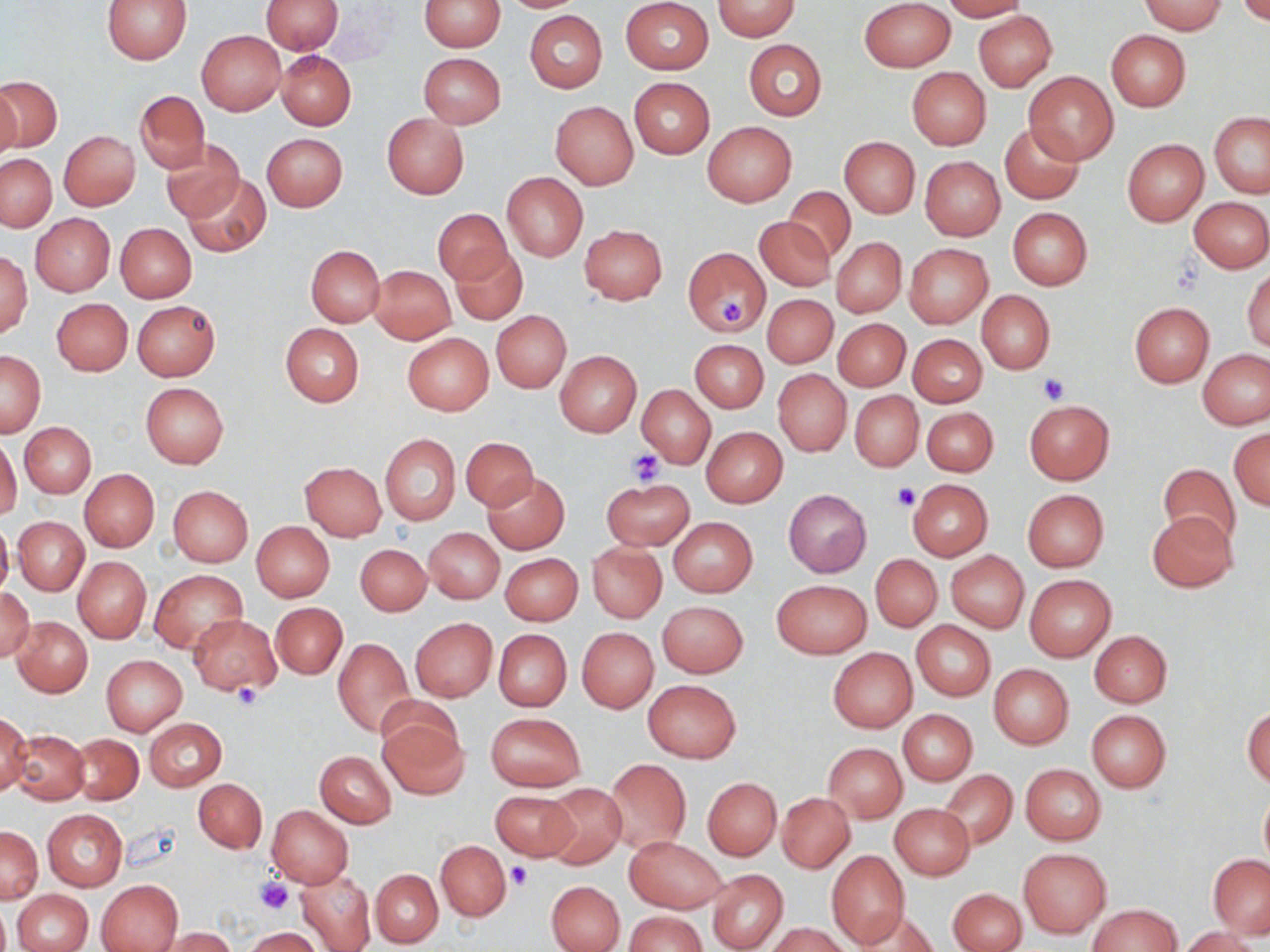

slide-level diagnosis = negative for blood parasites
stain = May-Grünwald-Giemsa
uninfected red blood cell locations = approximate bounding boxes as named x1/y1/x2/y2 corners in pixels: (x1=102, y1=0, x2=192, y2=64), (x1=261, y1=0, x2=344, y2=54), (x1=419, y1=0, x2=505, y2=51), (x1=497, y1=0, x2=591, y2=12), (x1=860, y1=0, x2=954, y2=71), (x1=942, y1=0, x2=1028, y2=21), (x1=621, y1=1, x2=713, y2=74), (x1=712, y1=1, x2=800, y2=39), (x1=1138, y1=1, x2=1227, y2=34), (x1=1235, y1=1, x2=1270, y2=24), (x1=524, y1=11, x2=606, y2=92), (x1=973, y1=11, x2=1057, y2=92), (x1=197, y1=30, x2=286, y2=115), (x1=1105, y1=30, x2=1190, y2=111), (x1=744, y1=40, x2=826, y2=121), (x1=275, y1=50, x2=356, y2=130), (x1=419, y1=53, x2=506, y2=127), (x1=907, y1=68, x2=991, y2=150), (x1=1023, y1=70, x2=1120, y2=164), (x1=0, y1=76, x2=61, y2=152), (x1=629, y1=77, x2=714, y2=158), (x1=0, y1=82, x2=20, y2=159), (x1=135, y1=90, x2=208, y2=172), (x1=550, y1=101, x2=638, y2=189), (x1=1209, y1=112, x2=1270, y2=198), (x1=382, y1=115, x2=469, y2=198), (x1=703, y1=122, x2=797, y2=206), (x1=1000, y1=122, x2=1084, y2=204), (x1=59, y1=130, x2=140, y2=211), (x1=262, y1=133, x2=348, y2=211), (x1=839, y1=137, x2=919, y2=219), (x1=161, y1=138, x2=245, y2=222), (x1=1121, y1=138, x2=1208, y2=226), (x1=1, y1=155, x2=56, y2=231), (x1=919, y1=156, x2=1006, y2=240), (x1=501, y1=172, x2=588, y2=261), (x1=182, y1=175, x2=270, y2=257), (x1=783, y1=185, x2=857, y2=263), (x1=1190, y1=197, x2=1270, y2=272), (x1=1007, y1=207, x2=1093, y2=290), (x1=434, y1=208, x2=513, y2=284), (x1=30, y1=213, x2=115, y2=297), (x1=756, y1=215, x2=835, y2=291), (x1=115, y1=223, x2=197, y2=303), (x1=579, y1=224, x2=668, y2=304), (x1=832, y1=238, x2=906, y2=317), (x1=904, y1=243, x2=993, y2=328), (x1=306, y1=244, x2=385, y2=327), (x1=451, y1=245, x2=527, y2=325), (x1=683, y1=246, x2=771, y2=336), (x1=1, y1=249, x2=32, y2=339), (x1=370, y1=265, x2=455, y2=343), (x1=1243, y1=269, x2=1270, y2=353), (x1=977, y1=290, x2=1055, y2=374), (x1=763, y1=294, x2=838, y2=368), (x1=53, y1=299, x2=132, y2=375), (x1=132, y1=301, x2=220, y2=381), (x1=1129, y1=302, x2=1214, y2=387), (x1=492, y1=311, x2=570, y2=392), (x1=832, y1=318, x2=909, y2=391), (x1=281, y1=323, x2=364, y2=407), (x1=402, y1=332, x2=493, y2=415), (x1=909, y1=333, x2=987, y2=406), (x1=690, y1=340, x2=768, y2=412), (x1=1199, y1=349, x2=1270, y2=429), (x1=1, y1=350, x2=45, y2=437), (x1=555, y1=351, x2=641, y2=437), (x1=773, y1=370, x2=851, y2=455), (x1=140, y1=382, x2=229, y2=468), (x1=637, y1=384, x2=715, y2=467), (x1=851, y1=391, x2=923, y2=471), (x1=1023, y1=399, x2=1115, y2=484), (x1=922, y1=407, x2=996, y2=477), (x1=20, y1=422, x2=96, y2=497), (x1=701, y1=426, x2=787, y2=507), (x1=1229, y1=428, x2=1269, y2=511), (x1=380, y1=434, x2=460, y2=525), (x1=0, y1=437, x2=21, y2=518), (x1=460, y1=438, x2=539, y2=510), (x1=301, y1=462, x2=387, y2=539), (x1=1158, y1=464, x2=1242, y2=550), (x1=79, y1=468, x2=159, y2=553), (x1=482, y1=471, x2=569, y2=553), (x1=600, y1=477, x2=694, y2=549), (x1=907, y1=479, x2=993, y2=561), (x1=168, y1=486, x2=252, y2=568), (x1=1022, y1=489, x2=1109, y2=572), (x1=783, y1=490, x2=872, y2=576), (x1=1146, y1=511, x2=1238, y2=593), (x1=0, y1=517, x2=12, y2=598), (x1=13, y1=517, x2=89, y2=596), (x1=669, y1=517, x2=758, y2=597), (x1=251, y1=521, x2=334, y2=602), (x1=424, y1=528, x2=504, y2=603), (x1=588, y1=542, x2=667, y2=623), (x1=355, y1=543, x2=431, y2=615), (x1=946, y1=551, x2=1028, y2=632), (x1=500, y1=553, x2=582, y2=626), (x1=871, y1=554, x2=942, y2=631), (x1=73, y1=557, x2=151, y2=642), (x1=149, y1=569, x2=248, y2=652), (x1=1024, y1=575, x2=1115, y2=660), (x1=773, y1=580, x2=871, y2=659), (x1=0, y1=587, x2=35, y2=660), (x1=657, y1=601, x2=748, y2=678), (x1=270, y1=602, x2=347, y2=679), (x1=188, y1=614, x2=280, y2=695), (x1=12, y1=616, x2=92, y2=697), (x1=411, y1=618, x2=497, y2=701), (x1=911, y1=621, x2=996, y2=701), (x1=577, y1=627, x2=658, y2=712), (x1=494, y1=629, x2=571, y2=710), (x1=1089, y1=630, x2=1172, y2=707), (x1=333, y1=638, x2=415, y2=737), (x1=828, y1=647, x2=917, y2=733), (x1=102, y1=654, x2=187, y2=736), (x1=988, y1=663, x2=1074, y2=749), (x1=643, y1=680, x2=740, y2=762), (x1=374, y1=705, x2=466, y2=798), (x1=1243, y1=705, x2=1270, y2=789), (x1=898, y1=709, x2=977, y2=786), (x1=1087, y1=709, x2=1171, y2=792), (x1=0, y1=712, x2=31, y2=794), (x1=485, y1=712, x2=584, y2=792), (x1=145, y1=718, x2=227, y2=791), (x1=10, y1=730, x2=88, y2=804), (x1=69, y1=734, x2=143, y2=803), (x1=823, y1=743, x2=906, y2=822), (x1=315, y1=750, x2=396, y2=828), (x1=605, y1=758, x2=691, y2=853), (x1=1020, y1=764, x2=1106, y2=845), (x1=940, y1=770, x2=1018, y2=849), (x1=702, y1=777, x2=781, y2=860), (x1=194, y1=778, x2=267, y2=852), (x1=540, y1=781, x2=627, y2=868), (x1=1259, y1=788, x2=1270, y2=870), (x1=490, y1=790, x2=579, y2=862), (x1=776, y1=791, x2=854, y2=872), (x1=890, y1=803, x2=975, y2=881), (x1=266, y1=805, x2=353, y2=888), (x1=42, y1=809, x2=127, y2=891), (x1=1, y1=827, x2=42, y2=903), (x1=625, y1=836, x2=728, y2=913), (x1=436, y1=840, x2=510, y2=921), (x1=1019, y1=848, x2=1110, y2=937), (x1=826, y1=850, x2=909, y2=948), (x1=1208, y1=854, x2=1270, y2=938), (x1=371, y1=869, x2=443, y2=947), (x1=706, y1=869, x2=788, y2=952), (x1=297, y1=871, x2=377, y2=952), (x1=96, y1=879, x2=182, y2=951), (x1=546, y1=880, x2=625, y2=952), (x1=12, y1=888, x2=93, y2=952), (x1=949, y1=889, x2=1024, y2=951), (x1=0, y1=901, x2=10, y2=952), (x1=1088, y1=904, x2=1183, y2=951), (x1=861, y1=909, x2=941, y2=951), (x1=624, y1=911, x2=707, y2=952), (x1=768, y1=922, x2=851, y2=952), (x1=1177, y1=927, x2=1262, y2=952), (x1=161, y1=928, x2=237, y2=952), (x1=243, y1=928, x2=323, y2=952)
magnification = 1000x
modality = light microscopy
platelet locations = approximate bounding boxes as named x1/y1/x2/y2 corners in pixels: (x1=716, y1=297, x2=753, y2=330), (x1=1037, y1=375, x2=1068, y2=405), (x1=626, y1=448, x2=667, y2=484), (x1=891, y1=481, x2=922, y2=509), (x1=230, y1=681, x2=264, y2=710), (x1=505, y1=864, x2=531, y2=889), (x1=253, y1=877, x2=294, y2=914)
image size = 1270×952 pixels
field of view = single
preparation = thin blood smear